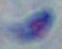 Toxoplasma gondii is shown. 1000x magnification. Photomicrograph.